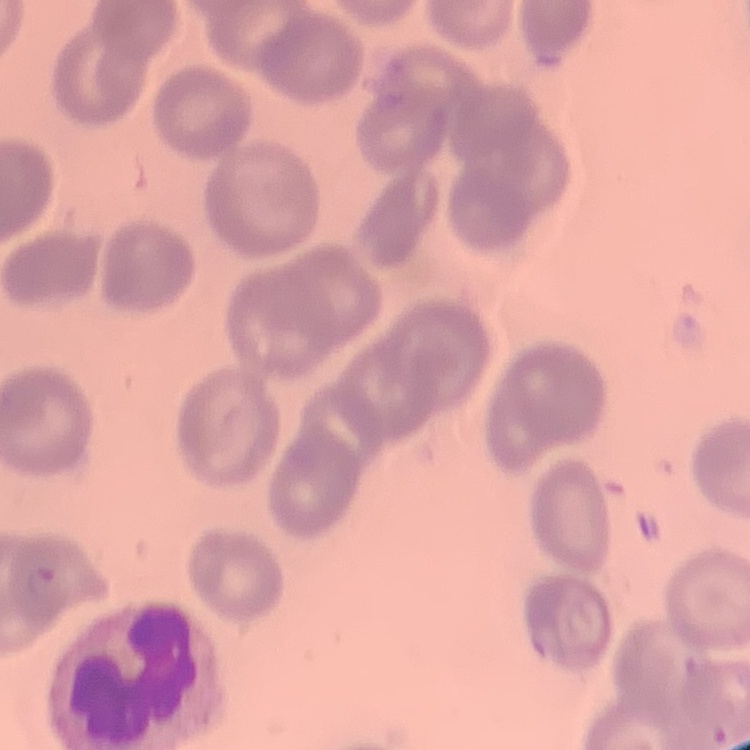 The erythrocytes exhibit no rouleaux formation. Stained with either Field's or Giemsa. One tile cut from a larger photomicrograph. Thin blood film.